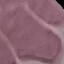

Summary:
  - Malaria status: uninfected
  - Capture: smartphone camera at the microscope eyepiece
  - Preparation: thin blood smear
  - Image type: cell patch, automatically extracted from a larger field of view and resized to 64 × 64 pixels
  - Stain: Giemsa